Identify the preparation type.
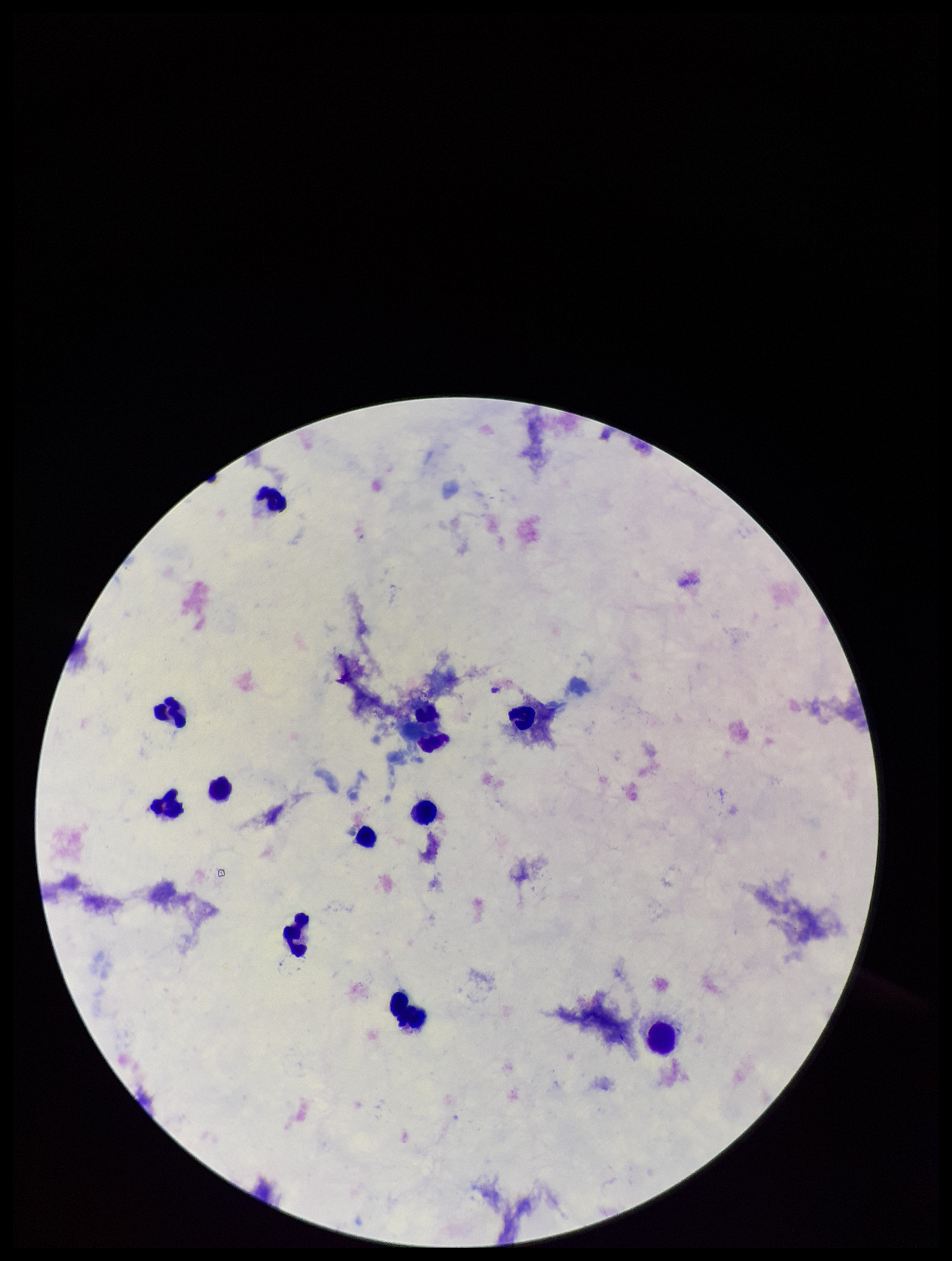
A thick smear.

{
  "parasite_count": 0,
  "stain": "Giemsa",
  "leukocyte_count": 10,
  "patient_malaria_status": "negative",
  "field_of_view": "one from this slide",
  "plasmodium_parasites": "none identified",
  "capture": "smartphone photograph through the microscope eyepiece",
  "image_size": "952×1261 pixels"
}